Assess this cell for malaria.
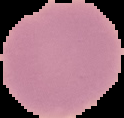

Uninfected.

The area outside the segmented cell region is set to black. Image is 124×118 pixels. From a thin blood smear.